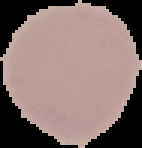
Summary:
  - Malaria status: uninfected
  - Image size: 142×148 pixels
  - Preparation: thin blood smear
  - Image type: segmented cell region with the area outside set to black